Assess for Plasmodium parasites.
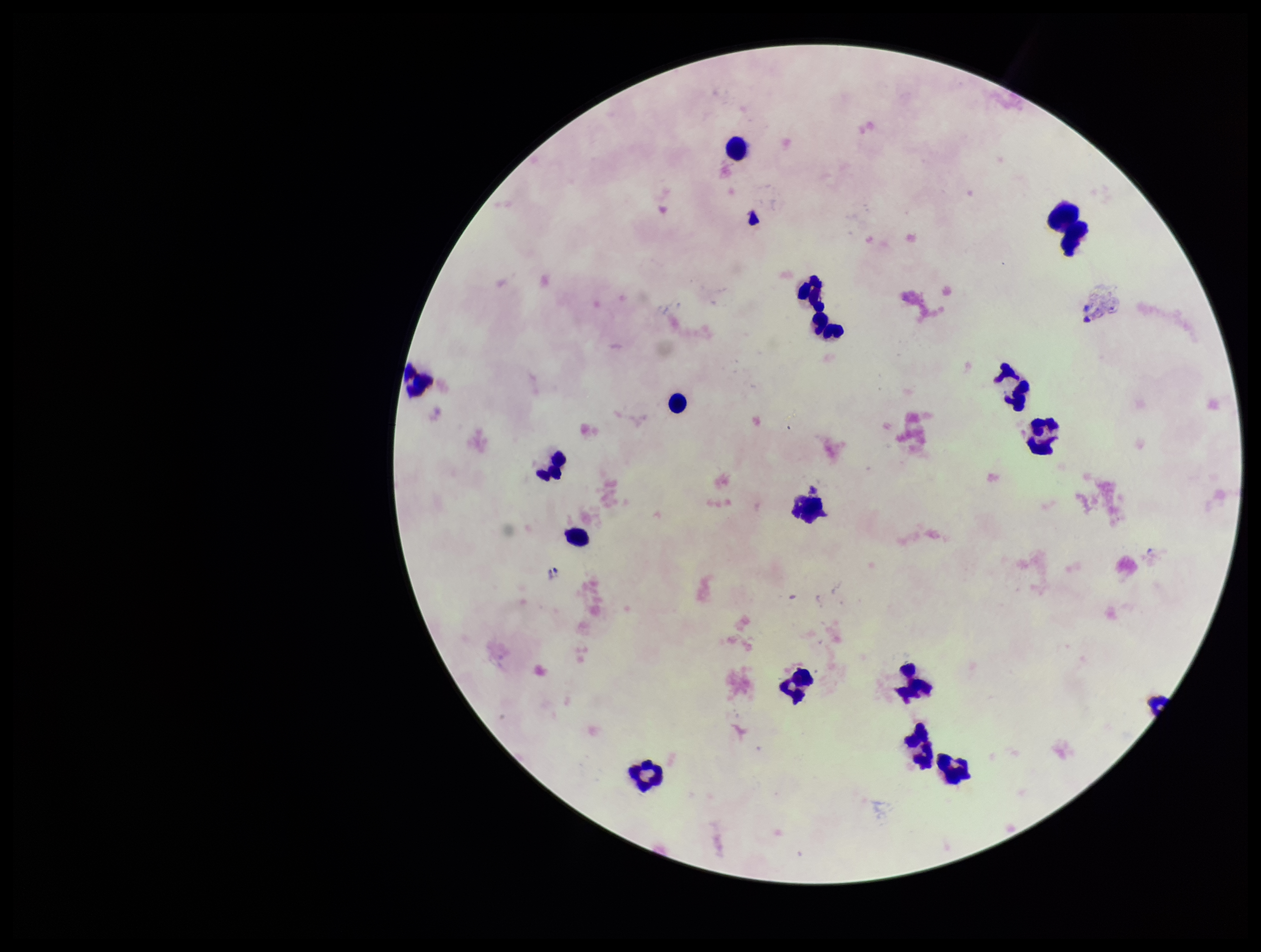

None seen.

Image is 1261×952 pixels. Parasite count: 0. Preparation: thick blood smear. Patient malaria status: negative. One field from this slide. Photographed through the microscope eyepiece with a smartphone camera. Giemsa stain. Leukocyte count: 18.